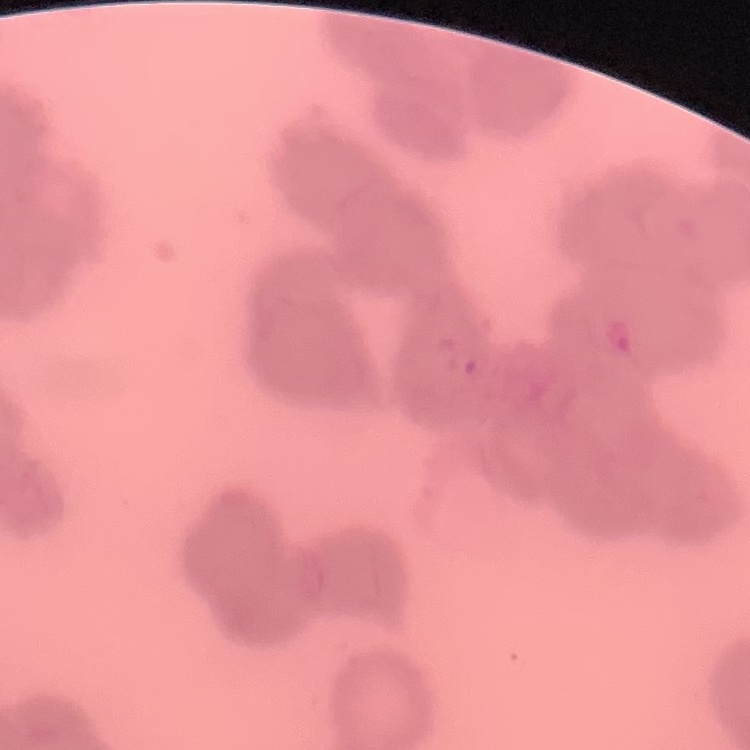 The red blood cells show rouleaux formation. Field's or Giemsa stain. Square crop of a larger photomicrograph. Thin peripheral smear.